Outline each white blood cell.
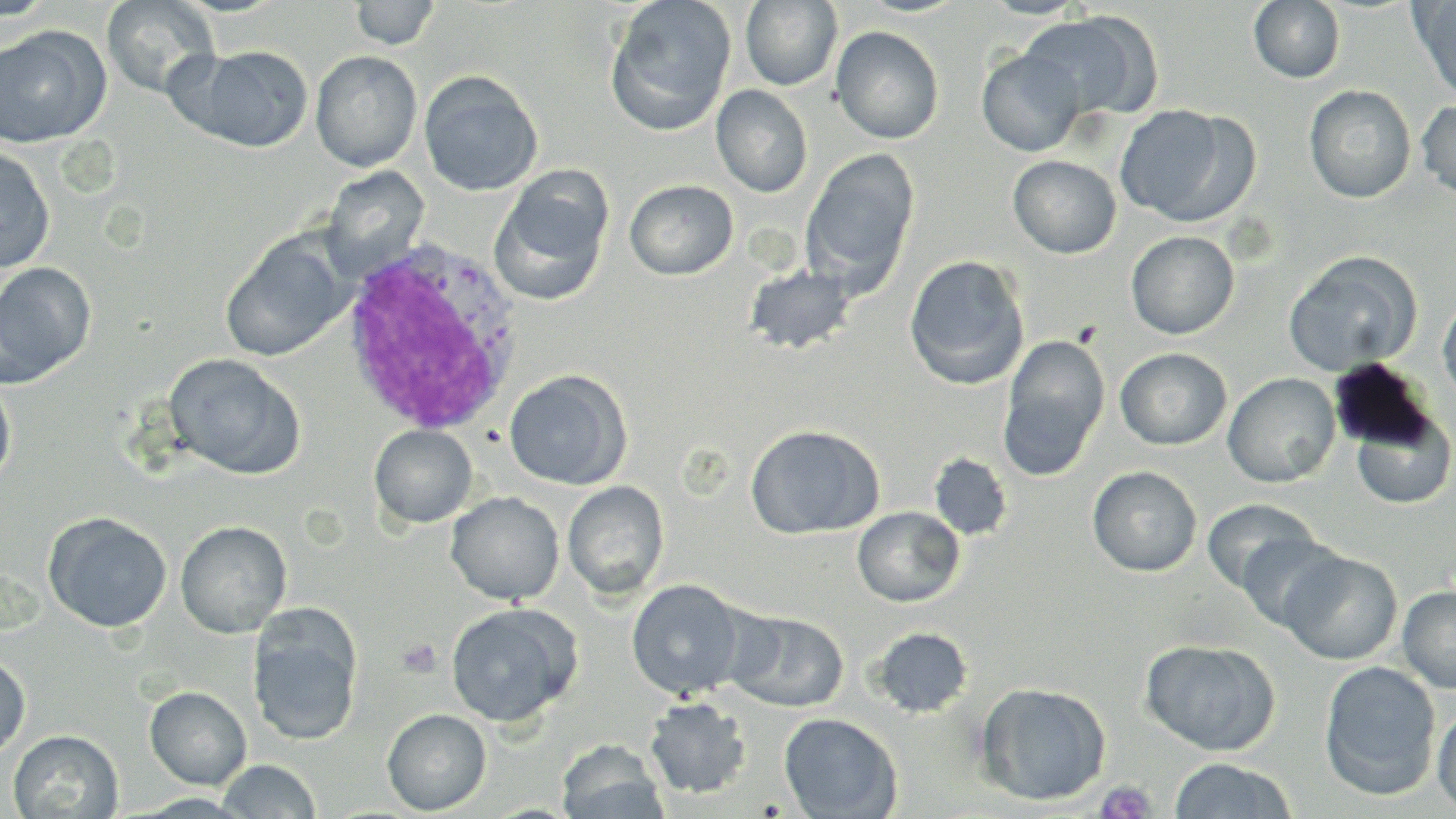
Approximate bounding boxes as (x1,y1)-(x2,y2) corner pairs in pixels.
White blood cells: (337,237)-(525,440).

slide-level diagnosis = Plasmodium ovale
image size = 1456×819 pixels
platelet locations = approximate bounding boxes as (x1,y1)-(x2,y2) corner pairs in pixels: (397,638)-(444,677), (1096,781)-(1157,819)
stain = May-Grünwald-Giemsa
uninfected red blood cell locations = approximate bounding boxes as (x1,y1)-(x2,y2) corner pairs in pixels: (1,0)-(54,22), (604,0)-(737,136), (978,0)-(1091,18), (1410,0)-(1456,102), (101,1)-(219,99), (348,1)-(440,50), (741,1)-(842,90), (1249,1)-(1345,83), (1019,11)-(1161,122), (830,25)-(944,144), (0,28)-(107,147), (186,45)-(313,152), (977,48)-(1087,157), (310,50)-(422,172), (418,70)-(543,196), (711,85)-(813,198), (1304,85)-(1416,203), (1416,99)-(1456,199), (1115,105)-(1253,228), (0,146)-(55,274), (801,149)-(920,295), (1008,155)-(1122,259), (318,166)-(431,278), (490,167)-(614,307), (624,179)-(739,280), (1125,231)-(1239,339), (221,233)-(351,362), (1282,251)-(1421,376), (904,255)-(1030,390), (0,262)-(95,387), (744,263)-(856,354), (1437,294)-(1456,406), (998,333)-(1110,481), (1115,347)-(1232,450), (164,353)-(305,480), (504,369)-(631,490), (1223,372)-(1341,488), (0,377)-(16,488), (1349,405)-(1456,510), (745,423)-(884,540), (369,424)-(478,528), (929,453)-(1013,541), (1088,466)-(1202,576), (563,480)-(670,600), (446,491)-(565,605), (1201,498)-(1319,594), (852,506)-(965,607), (43,511)-(172,633), (175,520)-(292,637), (1234,532)-(1346,631), (1279,550)-(1403,665), (626,579)-(748,700), (1397,585)-(1456,694), (444,603)-(580,728), (248,608)-(363,747), (728,610)-(849,713), (870,627)-(973,718), (1140,638)-(1280,755), (0,653)-(30,760), (1319,660)-(1441,801), (975,682)-(1111,806), (145,686)-(252,790), (645,697)-(752,799), (1432,705)-(1456,814), (382,709)-(491,815), (779,712)-(902,818), (8,730)-(123,817), (557,740)-(669,819), (1168,757)-(1297,818), (216,759)-(322,818)
preparation = thin blood film
modality = optical microscopy
field of view = single
magnification = 1000x